Report the malaria status of this cell.
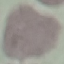

Uninfected.

{
  "image_type": "cell patch, automatically extracted from a larger field of view and resized to 64 × 64 pixels",
  "stain": "Giemsa",
  "preparation": "thin blood film",
  "capture": "smartphone camera at the microscope eyepiece"
}